Classify this cell by malaria status.
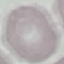
It is uninfected.

Acquired by smartphone through the microscope eyepiece. Automatically extracted cell patch, resized to 64 × 64 pixels. Thin smear of blood. Giemsa-stained preparation.